Outline each Trypanosoma brucei.
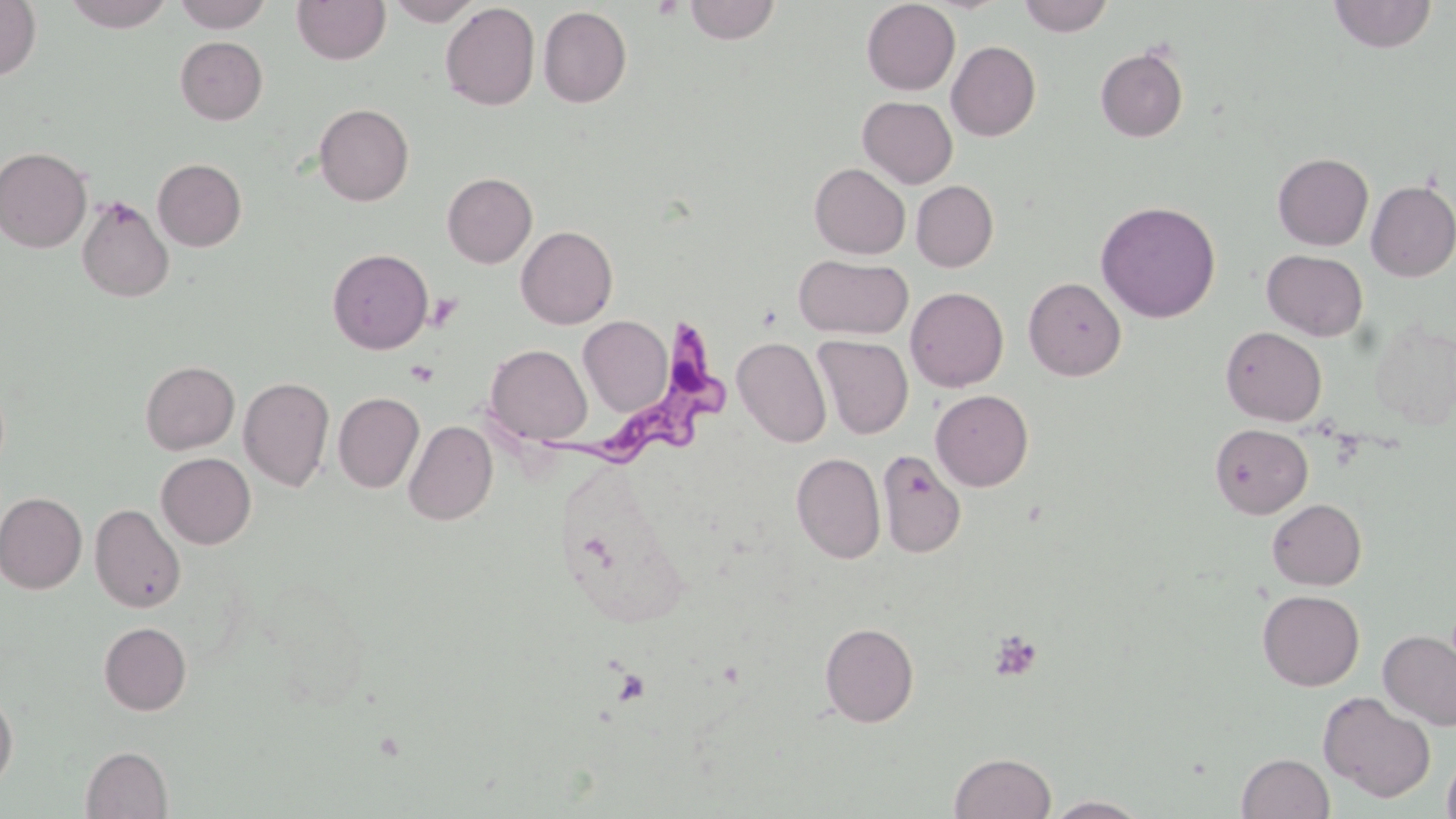

Approximate bounding boxes as (x1,y1)-(x2,y2) corner pairs in pixels.
Trypanosoma brucei: (540,316)-(739,473).

Summary:
  - Platelet locations: (653,0)-(684,21), (424,292)-(462,331), (405,360)-(438,386), (988,630)-(1043,681), (611,668)-(652,707)
  - Uninfected red blood cell locations: (0,0)-(42,81), (62,0)-(176,31), (173,0)-(272,32), (292,0)-(390,65), (385,0)-(484,26), (1018,0)-(1114,36), (1328,0)-(1437,53), (683,1)-(781,44), (861,1)-(960,95), (440,2)-(540,111), (538,6)-(632,108), (175,36)-(267,124), (946,41)-(1041,141), (1095,47)-(1188,142), (857,96)-(957,188), (314,104)-(413,206), (0,147)-(92,253), (1272,153)-(1373,250), (152,158)-(247,251), (810,163)-(910,259), (442,172)-(537,268), (911,180)-(998,271), (1366,180)-(1456,281), (76,196)-(174,302), (1096,200)-(1221,323), (516,226)-(618,329), (327,248)-(433,354), (1262,250)-(1368,341), (794,254)-(912,339), (1023,277)-(1126,381), (905,287)-(1008,392), (578,315)-(673,417), (1220,326)-(1327,426), (813,335)-(913,439), (733,336)-(832,448), (485,344)-(592,445), (140,360)-(239,454), (148,362)-(245,549), (239,377)-(335,491), (931,390)-(1034,491), (333,392)-(424,492), (404,420)-(498,525), (1210,423)-(1312,518), (877,450)-(966,558), (156,453)-(256,548), (792,453)-(885,564), (0,491)-(87,594), (1267,498)-(1366,589), (90,504)-(185,613), (1257,590)-(1364,691), (98,622)-(191,715), (820,622)-(919,727), (1378,631)-(1456,730), (0,691)-(17,794), (1318,691)-(1436,802), (80,746)-(173,819), (1441,747)-(1456,819), (949,752)-(1056,819), (1237,752)-(1334,818), (1045,795)-(1150,818)
  - Slide-level diagnosis: Trypanosoma brucei
  - Field of view: single
  - Stain: May-Grünwald-Giemsa
  - Modality: light microscopy
  - Magnification: 1000x
  - Image size: 1456×819 pixels
  - Preparation: thin blood film